Locate every Plasmodium ovale-infected red blood cell.
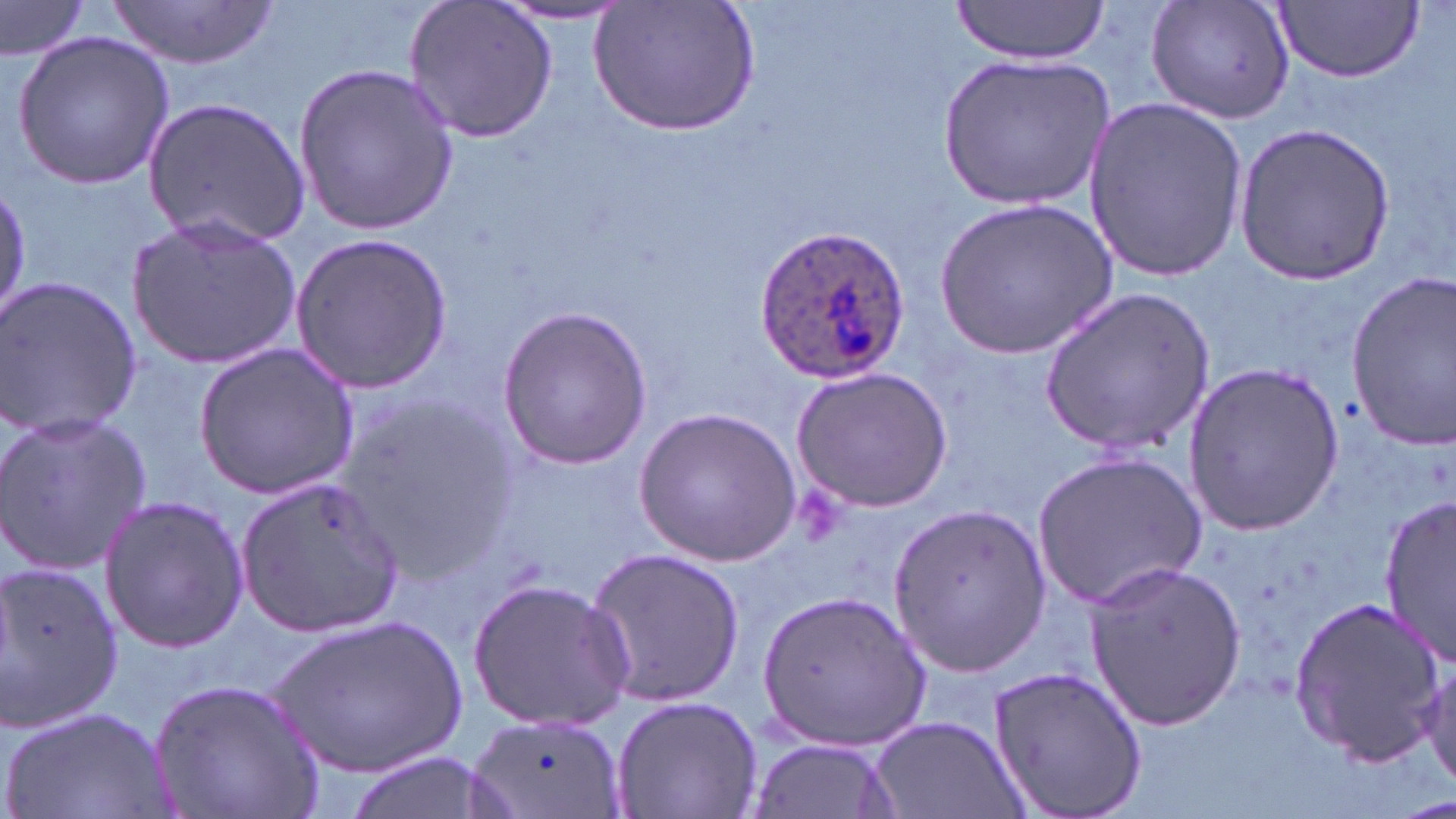
Approximate bounding boxes as (x1, y1, x2, y2) in pixels.
Plasmodium ovale-infected red blood cells: (748, 225, 911, 385).

slide_level_diagnosis: Plasmodium ovale
image_size: 1456×819 pixels
uninfected_red_blood_cell_locations: 'approximate bounding boxes as (x1, y1, x2, y2) in pixels: (106, 0, 279, 70), (1146, 0, 1297, 126), (405, 1, 560, 143), (949, 1, 1110, 63), (1272, 2, 1423, 83), (593, 3, 760, 136), (0, 4, 89, 65), (487, 5, 635, 26), (13, 31, 173, 189), (941, 52, 1115, 208), (293, 61, 458, 233), (1084, 95, 1248, 279), (143, 97, 311, 250), (1231, 121, 1396, 284), (1, 181, 29, 323), (934, 195, 1117, 357), (124, 212, 302, 373), (287, 232, 454, 392), (1343, 270, 1456, 452), (0, 275, 144, 442), (1040, 284, 1218, 459), (496, 305, 653, 469), (193, 342, 359, 499), (1181, 362, 1346, 535), (791, 365, 954, 513), (332, 392, 516, 573), (633, 406, 801, 566), (0, 409, 152, 577), (1030, 449, 1206, 610), (235, 478, 402, 639), (1378, 493, 1455, 667), (98, 495, 250, 653), (887, 505, 1053, 673), (583, 544, 746, 710), (1084, 559, 1248, 734), (0, 560, 124, 736), (467, 577, 636, 732), (756, 587, 932, 750), (1288, 596, 1445, 767), (270, 614, 472, 777), (1421, 653, 1455, 794), (985, 663, 1147, 819), (149, 676, 328, 819), (609, 694, 762, 819), (3, 705, 167, 819), (469, 713, 626, 819), (868, 713, 1030, 819), (744, 733, 900, 818), (339, 749, 505, 819)'
preparation: thin blood film
stain: May-Grünwald-Giemsa
modality: optical microscopy
magnification: 1000x
field_of_view: one of a larger specimen